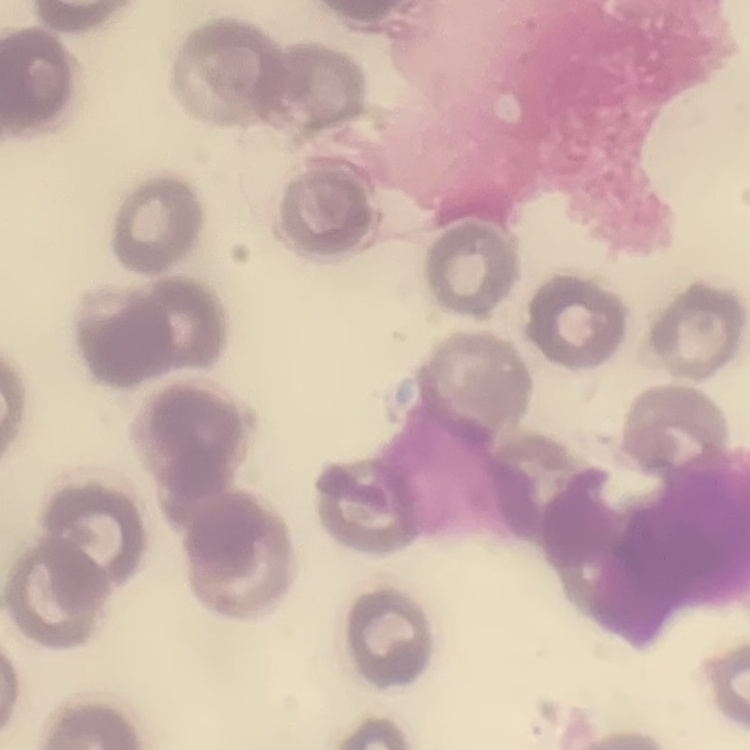
erythrocyte morphology = no rouleaux formation
image type = square crop of a larger photomicrograph
stain = Field's or Giemsa
preparation = thin peripheral smear